Identify the parasite.
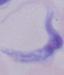
A trypanosome.

1000x magnification. Micrograph.